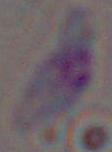
{
  "modality": "micrograph",
  "identification": "Toxoplasma gondii",
  "magnification": "1000x"
}